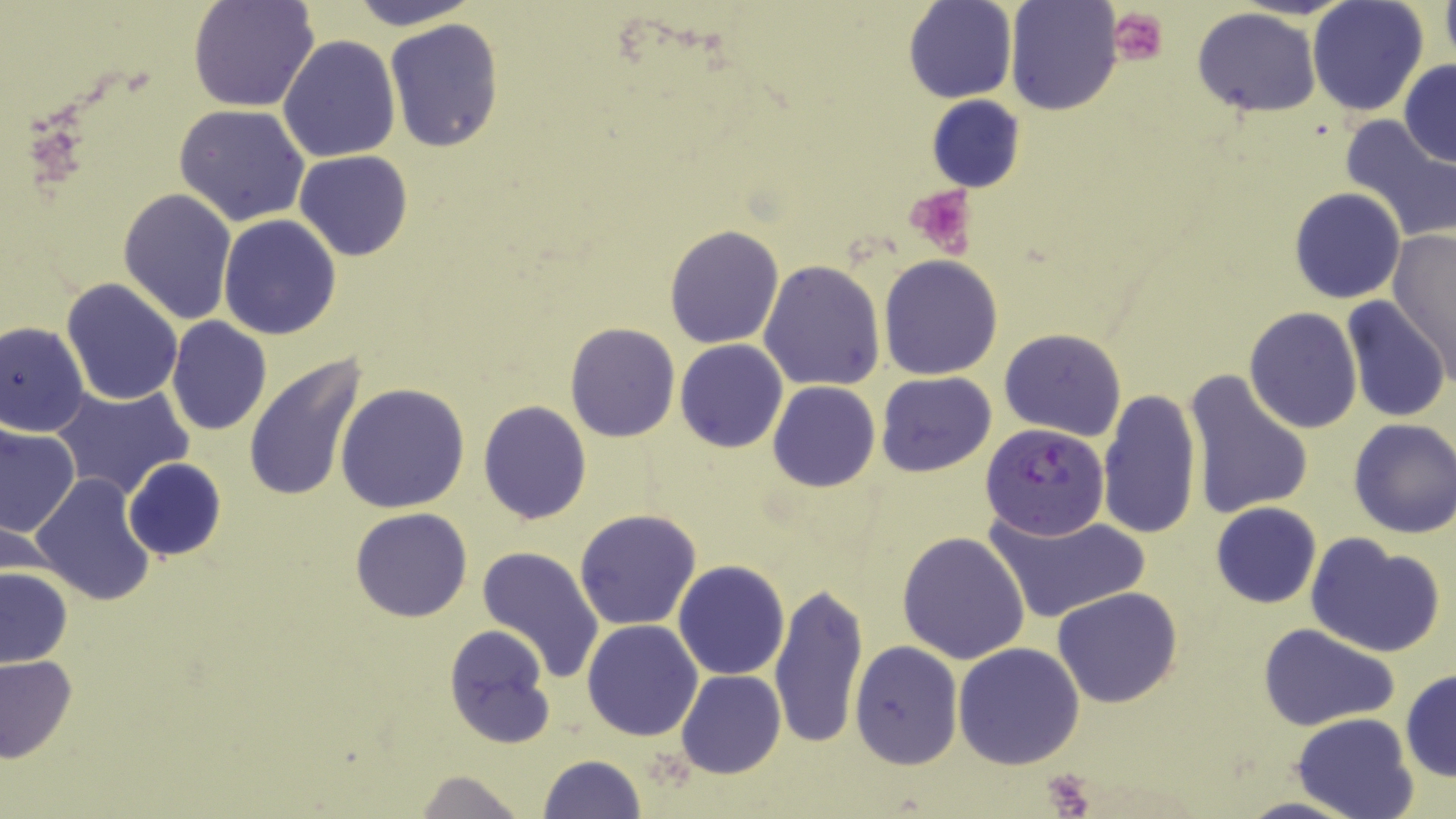
slide-level diagnosis = Plasmodium falciparum
platelet locations = approximate bounding boxes as named x1/y1/x2/y2 corners in pixels: (x1=1107, y1=7, x2=1168, y2=67), (x1=904, y1=185, x2=978, y2=258), (x1=1037, y1=769, x2=1100, y2=814)
Plasmodium falciparum-infected red blood cell locations = approximate bounding boxes as named x1/y1/x2/y2 corners in pixels: (x1=981, y1=422, x2=1111, y2=539)
field of view = one of a larger specimen
modality = optical microscopy
magnification = 1000x
uninfected red blood cell locations = approximate bounding boxes as named x1/y1/x2/y2 corners in pixels: (x1=188, y1=0, x2=319, y2=113), (x1=344, y1=0, x2=481, y2=30), (x1=903, y1=0, x2=1016, y2=103), (x1=1003, y1=0, x2=1122, y2=115), (x1=1306, y1=0, x2=1430, y2=118), (x1=1439, y1=0, x2=1456, y2=66), (x1=1193, y1=8, x2=1321, y2=117), (x1=384, y1=19, x2=504, y2=153), (x1=277, y1=35, x2=400, y2=161), (x1=1399, y1=59, x2=1456, y2=167), (x1=926, y1=95, x2=1026, y2=191), (x1=175, y1=104, x2=310, y2=226), (x1=1337, y1=114, x2=1456, y2=243), (x1=294, y1=150, x2=414, y2=261), (x1=1287, y1=187, x2=1405, y2=304), (x1=117, y1=188, x2=237, y2=326), (x1=218, y1=215, x2=342, y2=339), (x1=663, y1=225, x2=785, y2=348), (x1=1388, y1=229, x2=1454, y2=381), (x1=879, y1=255, x2=1003, y2=379), (x1=759, y1=259, x2=886, y2=391), (x1=60, y1=278, x2=184, y2=406), (x1=1341, y1=297, x2=1449, y2=422), (x1=1244, y1=307, x2=1362, y2=432), (x1=167, y1=317, x2=272, y2=435), (x1=1, y1=321, x2=91, y2=435), (x1=565, y1=322, x2=679, y2=442), (x1=999, y1=328, x2=1127, y2=441), (x1=676, y1=339, x2=788, y2=452), (x1=244, y1=353, x2=369, y2=504), (x1=1183, y1=370, x2=1314, y2=521), (x1=875, y1=371, x2=997, y2=476), (x1=767, y1=381, x2=880, y2=493), (x1=335, y1=382, x2=471, y2=514), (x1=50, y1=384, x2=195, y2=501), (x1=1097, y1=390, x2=1202, y2=540), (x1=478, y1=400, x2=592, y2=523), (x1=1346, y1=419, x2=1456, y2=539), (x1=0, y1=423, x2=80, y2=537), (x1=122, y1=457, x2=226, y2=562), (x1=29, y1=474, x2=157, y2=606), (x1=1210, y1=502, x2=1323, y2=609), (x1=351, y1=507, x2=472, y2=621), (x1=574, y1=508, x2=703, y2=630), (x1=982, y1=508, x2=1151, y2=625), (x1=897, y1=530, x2=1030, y2=665), (x1=1304, y1=532, x2=1445, y2=658), (x1=477, y1=546, x2=604, y2=683), (x1=673, y1=559, x2=790, y2=680), (x1=0, y1=563, x2=72, y2=668), (x1=769, y1=580, x2=870, y2=749), (x1=1052, y1=586, x2=1183, y2=708), (x1=582, y1=620, x2=704, y2=740), (x1=1260, y1=623, x2=1398, y2=731), (x1=442, y1=625, x2=557, y2=750), (x1=850, y1=641, x2=963, y2=771), (x1=953, y1=641, x2=1085, y2=770), (x1=0, y1=654, x2=79, y2=763), (x1=1400, y1=669, x2=1456, y2=782), (x1=677, y1=670, x2=785, y2=778), (x1=1292, y1=711, x2=1417, y2=819), (x1=537, y1=755, x2=648, y2=818), (x1=412, y1=770, x2=529, y2=819)
preparation = thin blood smear
stain = May-Grünwald-Giemsa
image size = 1456×819 pixels